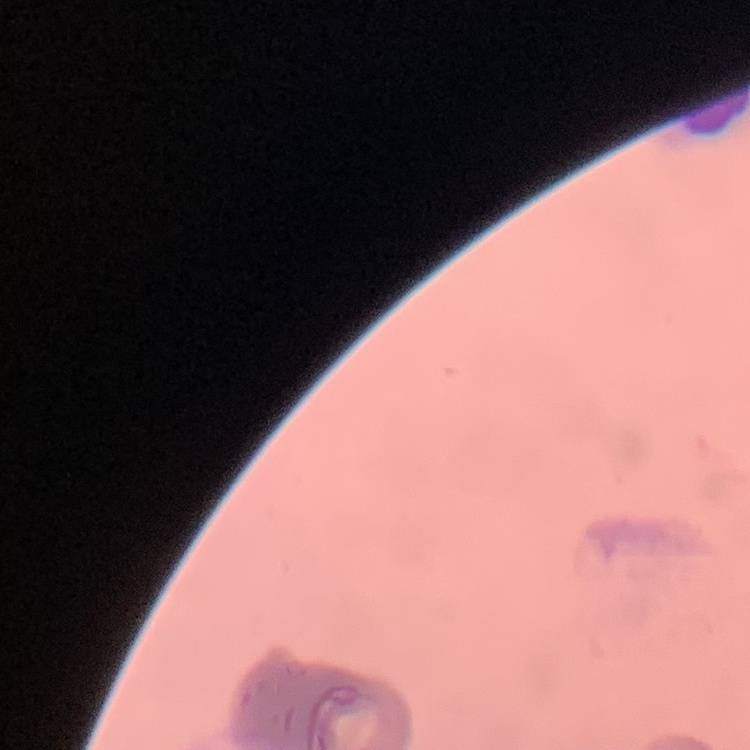
{
  "erythrocyte_morphology": "rouleaux formation",
  "stain": "Field's or Giemsa",
  "preparation": "thin blood smear",
  "image_type": "square crop of a larger photomicrograph"
}